Name the parasite shown.
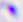
This is Toxoplasma gondii.

modality = photomicrograph
magnification = 400x